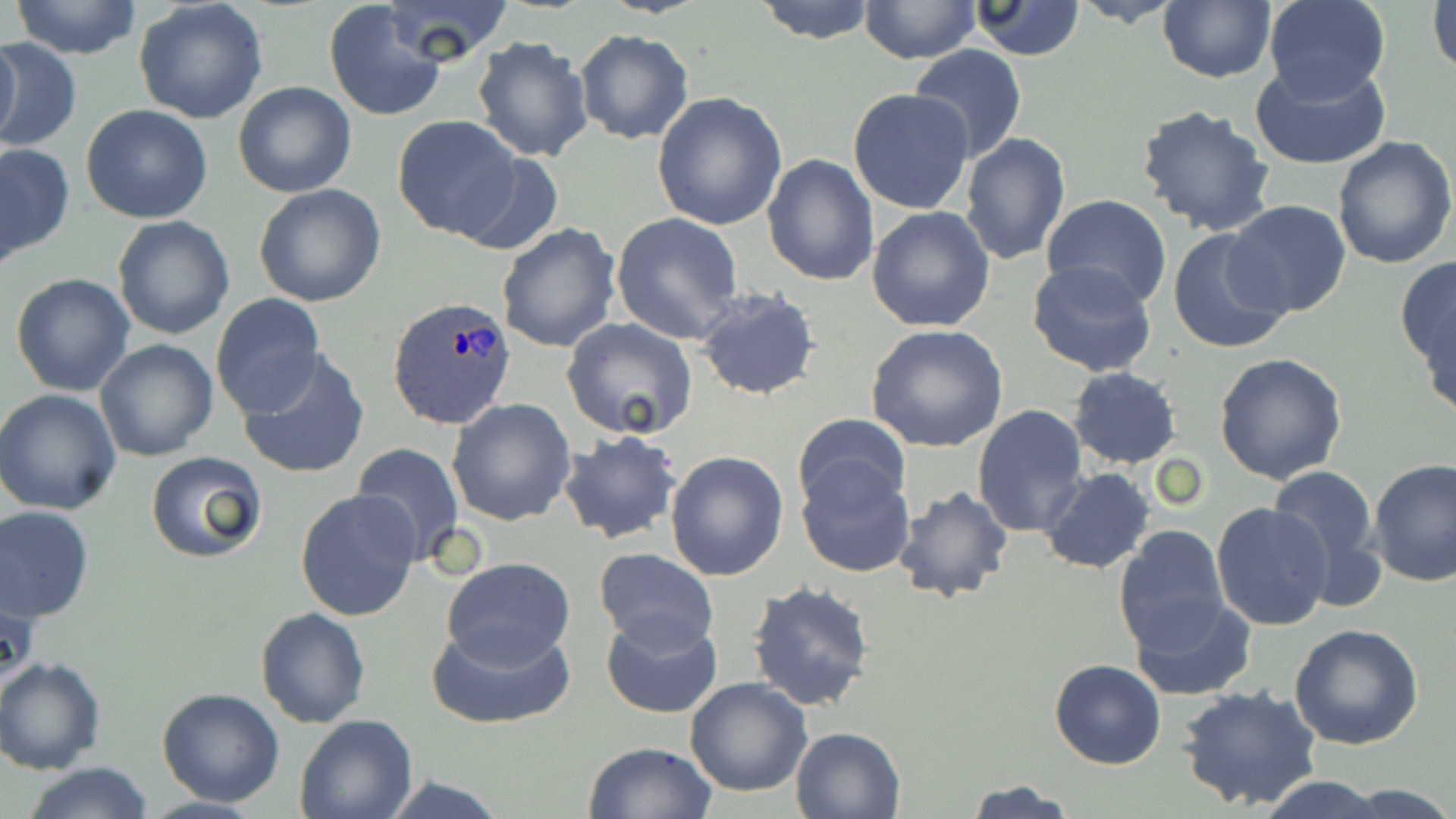
slide-level diagnosis = Plasmodium ovale
field of view = single
preparation = thin blood film
Plasmodium ovale-infected red blood cell locations = approximate bounding boxes as [x1, y1, x2, y2] in pixels: [388, 295, 518, 431]
image size = 1456×819 pixels
modality = optical microscopy
stain = May-Grünwald-Giemsa
uninfected red blood cell locations = approximate bounding boxes as [x1, y1, x2, y2] in pixels: [10, 0, 145, 59], [134, 0, 269, 124], [382, 0, 514, 65], [752, 0, 879, 44], [1071, 0, 1185, 27], [1263, 0, 1390, 104], [1428, 0, 1456, 79], [323, 1, 449, 123], [858, 1, 981, 65], [965, 1, 1087, 60], [1157, 2, 1275, 83], [573, 29, 695, 145], [471, 34, 594, 163], [0, 37, 22, 151], [1, 37, 80, 156], [909, 47, 1028, 163], [1248, 61, 1394, 168], [233, 81, 356, 198], [847, 88, 976, 215], [652, 92, 789, 232], [1136, 104, 1277, 237], [81, 105, 213, 223], [390, 115, 527, 242], [959, 131, 1070, 267], [1332, 136, 1454, 270], [0, 143, 74, 265], [452, 149, 565, 256], [763, 151, 881, 287], [252, 183, 387, 308], [1042, 195, 1171, 308], [1223, 200, 1353, 319], [867, 205, 996, 332], [611, 212, 745, 344], [113, 216, 236, 338], [496, 222, 621, 354], [1167, 229, 1294, 355], [1395, 254, 1456, 387], [1027, 259, 1158, 377], [10, 272, 135, 396], [694, 287, 822, 402], [210, 294, 326, 417], [561, 317, 698, 441], [865, 324, 1009, 452], [94, 338, 219, 462], [237, 348, 370, 480], [1214, 353, 1349, 485], [1067, 367, 1182, 469], [0, 388, 123, 515], [446, 398, 577, 525], [973, 404, 1088, 537], [790, 413, 912, 518], [558, 431, 684, 545], [351, 441, 469, 565], [663, 449, 789, 581], [144, 451, 267, 563], [1370, 460, 1456, 588], [796, 461, 915, 577], [1265, 466, 1382, 584], [1040, 467, 1156, 576], [891, 485, 1015, 605], [295, 488, 421, 623], [1210, 503, 1333, 633], [0, 505, 95, 622], [1113, 526, 1230, 652], [594, 548, 719, 653], [441, 557, 576, 667], [747, 580, 877, 714], [1131, 592, 1255, 700], [255, 607, 370, 728], [600, 612, 723, 719], [427, 620, 576, 730], [1290, 624, 1424, 751], [0, 656, 106, 775], [1049, 659, 1167, 769], [684, 676, 812, 797], [1179, 685, 1323, 812], [156, 688, 285, 807], [295, 713, 418, 819], [790, 725, 907, 818], [583, 741, 719, 819], [20, 762, 156, 819], [1253, 774, 1397, 818], [961, 778, 1081, 818], [1338, 782, 1455, 819]
magnification = 1000x